Give the position of every P. falciparum parasite, noting its life-cycle stage.
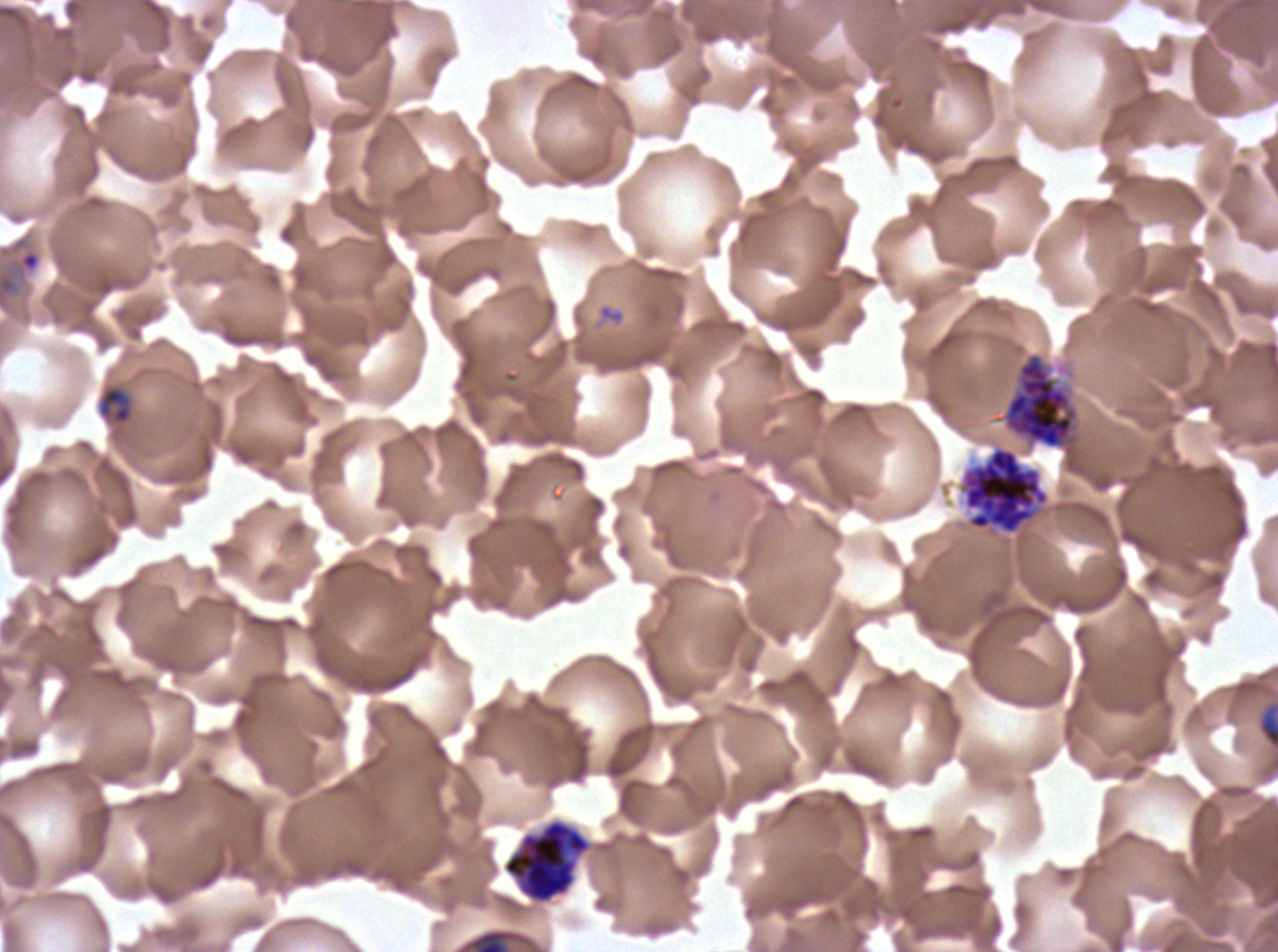
Approximate bounding boxes as [x1, y1, x2, y2] in pixels.
Rings: [0, 249, 42, 309].
Late-ring/early-trophozoite forms: [98, 385, 132, 424].
Segmenters: [1002, 353, 1078, 449], [958, 445, 1051, 536], [502, 818, 592, 905].
No mid trophozoites, late trophozoites, early schizonts, late schizonts, or gametocytes observed.

debris locations = [1258, 703, 1277, 750]
stain = Giemsa
preparation = thin blood film
image size = 1278×952 pixels
field of view = one sub-image of a larger composite
life-cycle stages observed = ring, late-ring/early-trophozoite, segmenter
specimen = P. falciparum from a patient in The Gambia, cultured ex vivo for 24 to 48 hours